Assess this cell for malaria.
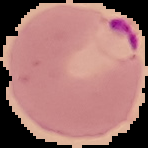

Parasitized.

preparation = thin blood film
image type = cell region segmented out of the field of view; surrounding area masked to black
image size = 148×148 pixels